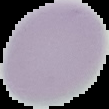

Summary:
  - Preparation: thin blood film
  - Image size: 109×109 pixels
  - Image type: segmented cell region with the area outside set to black
  - Result: no malaria parasites seen